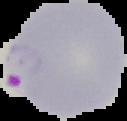

Summary:
  - Image size: 127×121 pixels
  - Preparation: thin blood smear
  - Image type: segmented cell region on a black background
  - Result: Plasmodium parasites identified